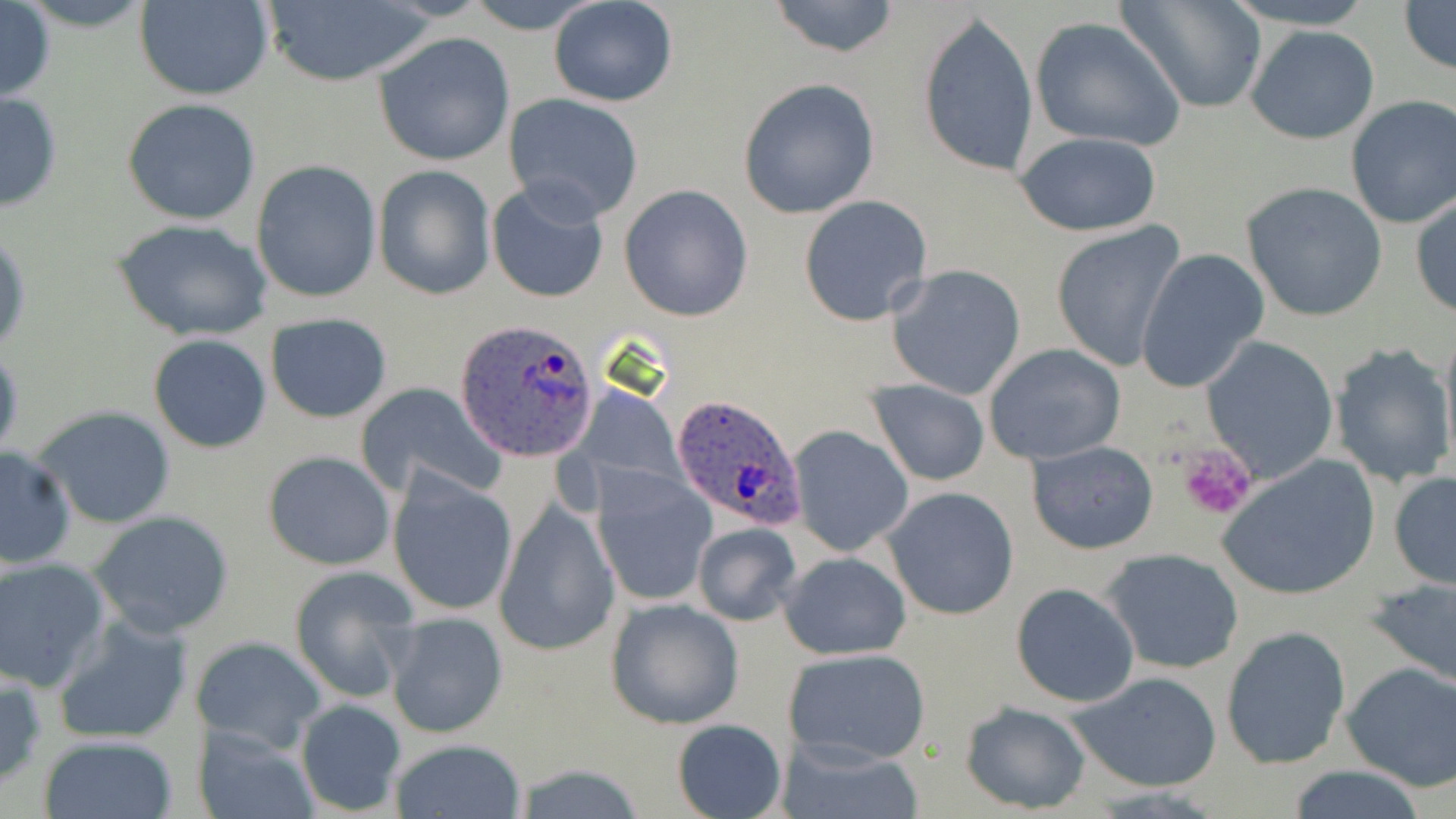 Approximate bounding boxes as [x1, y1, x2, y2] in pixels. Plasmodium ovale-infected red blood cell locations: [454, 320, 598, 465], [673, 389, 807, 528]. Platelet locations: [1175, 441, 1258, 522]. Uninfected red blood cell locations: [136, 0, 274, 99], [463, 0, 606, 33], [548, 0, 679, 107], [1118, 0, 1266, 115], [765, 1, 902, 58], [1398, 1, 1456, 74], [0, 2, 55, 105], [261, 2, 435, 85], [917, 11, 1039, 177], [1030, 16, 1185, 151], [1246, 25, 1380, 145], [373, 32, 516, 166], [736, 77, 881, 219], [0, 90, 62, 211], [503, 92, 645, 221], [1343, 95, 1455, 231], [121, 98, 262, 227], [1013, 131, 1163, 237], [251, 160, 382, 305], [373, 166, 495, 300], [486, 179, 611, 305], [1241, 181, 1389, 323], [619, 183, 754, 322], [1410, 194, 1456, 319], [798, 195, 933, 326], [113, 220, 270, 341], [1051, 222, 1186, 372], [1, 229, 31, 358], [1134, 248, 1270, 395], [884, 262, 1027, 401], [263, 311, 392, 423], [1439, 320, 1456, 469], [148, 334, 273, 453], [1199, 335, 1340, 485], [0, 339, 23, 469], [982, 342, 1128, 466], [1331, 344, 1454, 488], [865, 378, 991, 487], [354, 382, 501, 501], [34, 406, 177, 530], [788, 425, 914, 557], [1026, 439, 1159, 555], [0, 446, 76, 571], [262, 451, 397, 571], [1218, 455, 1381, 601], [590, 466, 716, 606], [1388, 470, 1456, 591], [388, 471, 518, 616], [883, 486, 1019, 620], [493, 498, 621, 657], [90, 510, 235, 639], [691, 523, 802, 627], [1101, 548, 1246, 676], [778, 551, 912, 661], [0, 558, 110, 693], [287, 565, 422, 705], [1362, 580, 1456, 691], [1010, 583, 1138, 709], [607, 598, 744, 730], [383, 611, 508, 740], [51, 612, 196, 747], [1221, 624, 1352, 770], [192, 634, 327, 753], [783, 647, 932, 766], [1340, 663, 1456, 791], [0, 666, 46, 788], [1067, 670, 1224, 791], [294, 699, 407, 816], [958, 700, 1093, 813], [671, 718, 787, 819], [194, 729, 319, 819], [38, 734, 180, 819], [388, 738, 527, 819], [779, 742, 920, 818], [507, 763, 649, 818], [1281, 766, 1435, 819]. Slide-level diagnosis: Plasmodium ovale. Thin blood smear. Single field of view. Light microscopy. 1000x magnification. May-Grünwald-Giemsa-stained preparation. Image is 1456×819 pixels.